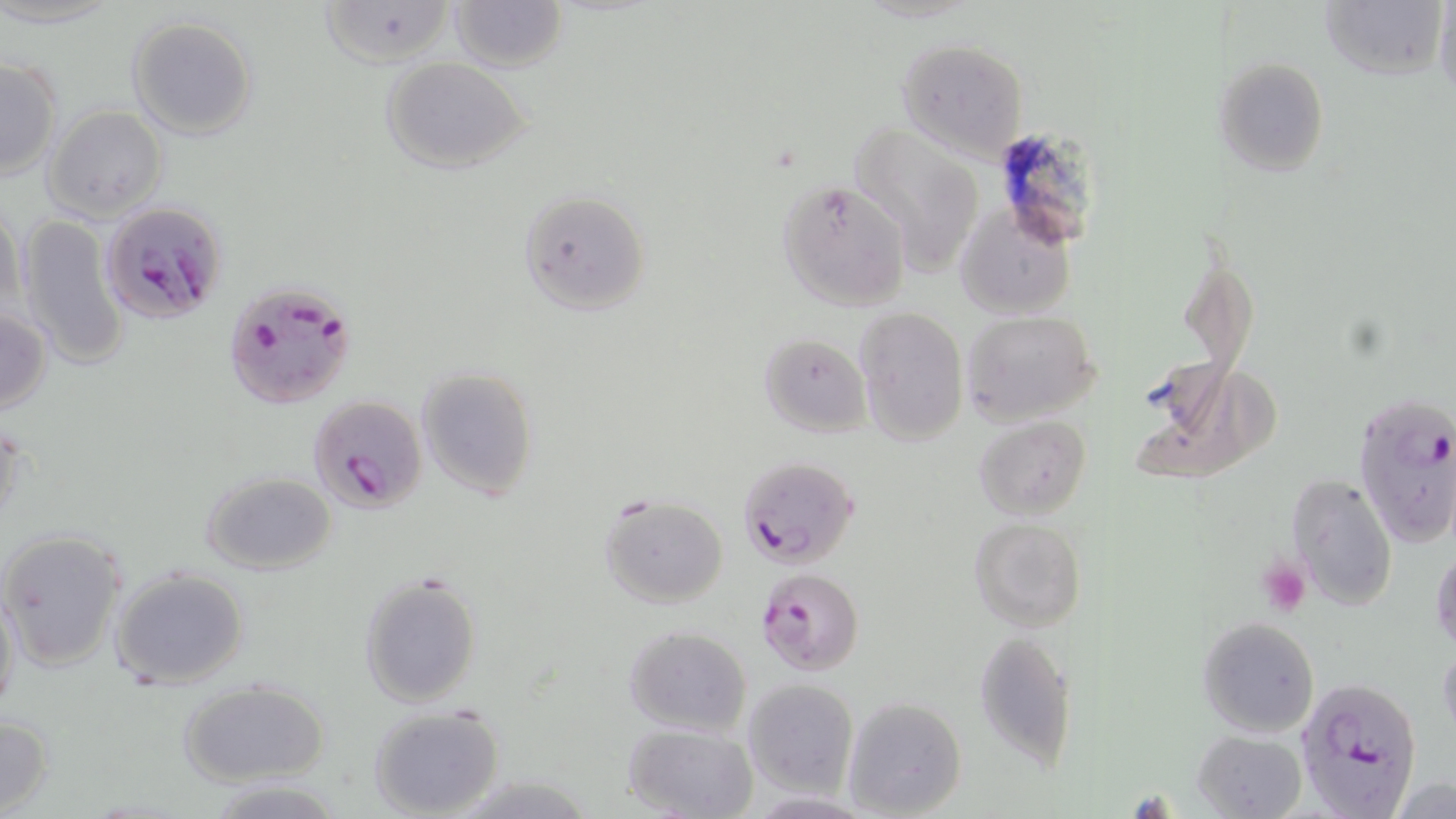 Approximate bounding boxes as [x1, y1, x2, y2] in pixels. Uninfected red blood cell locations: [322, 0, 453, 66], [448, 0, 568, 71], [1319, 1, 1446, 81], [1433, 2, 1456, 97], [127, 16, 257, 139], [896, 37, 1029, 162], [0, 56, 61, 180], [1212, 56, 1329, 177], [380, 57, 533, 175], [43, 106, 168, 221], [851, 124, 987, 277], [778, 178, 912, 311], [519, 190, 650, 316], [954, 201, 1076, 321], [1, 203, 29, 322], [15, 214, 131, 369], [0, 305, 52, 415], [854, 309, 969, 445], [962, 311, 1101, 428], [763, 332, 871, 437], [1130, 358, 1278, 489], [417, 366, 538, 500], [0, 414, 28, 535], [973, 416, 1091, 519], [201, 469, 337, 575], [1286, 471, 1399, 611], [599, 493, 728, 608], [969, 518, 1086, 633], [1, 529, 127, 670], [1431, 547, 1456, 654], [111, 566, 249, 690], [358, 570, 484, 709], [0, 579, 21, 719], [1196, 615, 1320, 740], [622, 625, 753, 737], [973, 628, 1077, 769], [1438, 638, 1456, 743], [178, 678, 329, 787], [740, 679, 858, 798], [843, 697, 967, 818], [368, 705, 506, 819], [0, 713, 53, 816], [621, 721, 758, 819], [1193, 730, 1307, 819], [1390, 776, 1453, 819], [210, 779, 348, 817], [747, 791, 876, 819]. Platelet locations: [1257, 557, 1310, 616]. Plasmodium falciparum-infected red blood cell locations: [102, 201, 228, 324], [221, 282, 353, 409], [307, 394, 428, 512], [1354, 394, 1456, 549], [736, 454, 860, 572], [755, 567, 864, 675], [1295, 678, 1425, 817]. Slide-level diagnosis: Plasmodium falciparum. May-Grünwald-Giemsa-stained preparation. Single field of view. Thin blood smear. Image is 1456×819 pixels. Optical microscopy. 1000x magnification.